Classify this cell by malaria status.
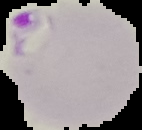
It is parasitized.

image size = 142×130 pixels
preparation = thin blood film
image type = segmented cell region on a black background